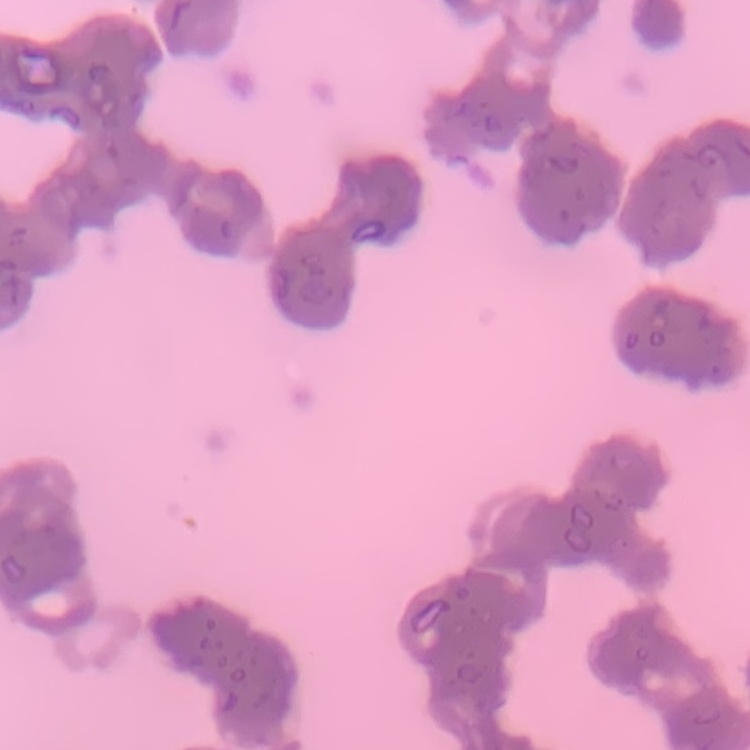 The erythrocytes show rouleaux formation. Field's or Giemsa stain. Thin blood film. Square crop of a larger photomicrograph.